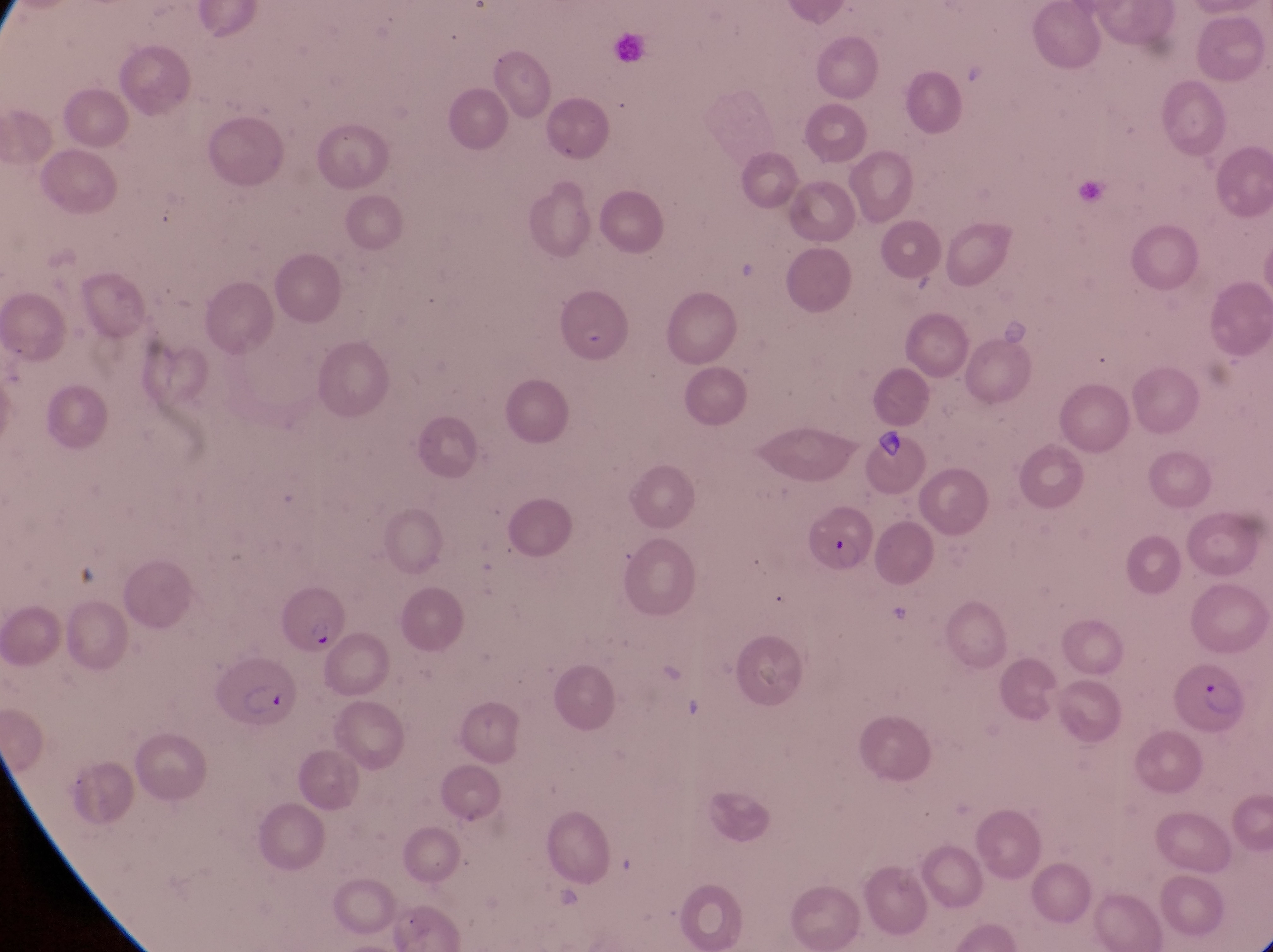
Approximate bounding boxes as {left, top, right, bottom} in pixels.
Summary:
  - Parasitised red blood cell locations: {559, 290, 644, 373}, {806, 504, 876, 579}, {213, 657, 301, 739}, {1174, 662, 1244, 742}
  - Magnification: 1000x
  - Country: Uganda
  - Preparation: thin blood film
  - Field of view: single
  - Image size: 1273×952 pixels
  - Capture: smartphone photograph through the eyepiece of an Olympus CX-23 microscope